Report the malaria status of this cell.
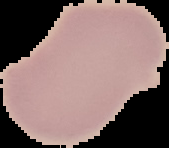
Uninfected.

From a thin blood film. Image is 169×148 pixels. Segmented cell region on a black background.